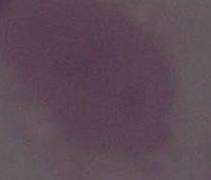 Photomicrograph. 1000x magnification. An erythrocyte is shown.